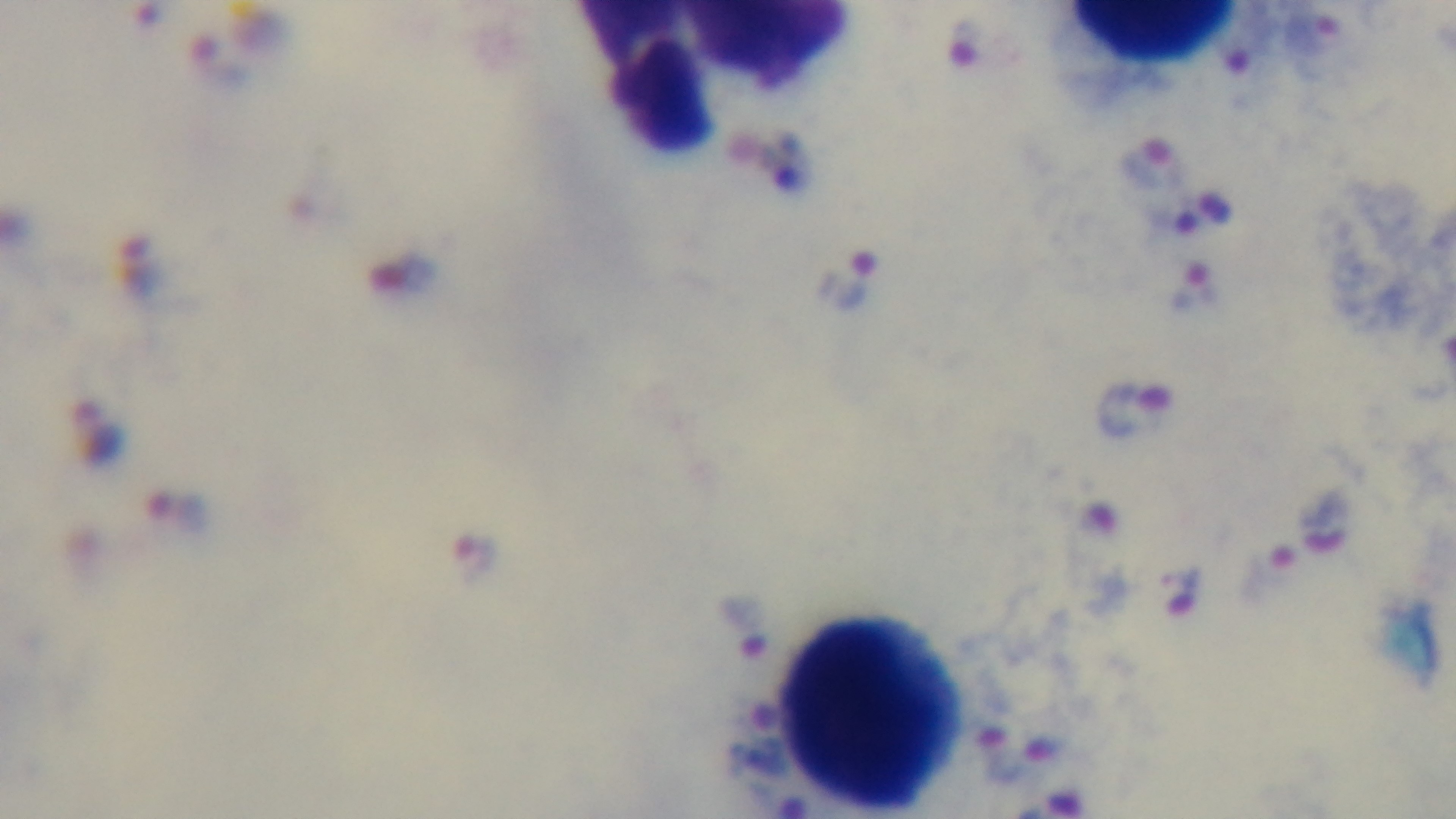

Summary:
  - Capture: mounted 4K digital camera
  - Stain: Giemsa
  - Field of view: one from the slide
  - Malaria status: positive
  - Modality: light microscopy
  - Preparation: thick smear
  - Objective: 100x oil immersion